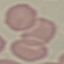
Malaria status: uninfected. Giemsa stain. Cell patch, automatically extracted from a larger field of view and resized to 64 × 64 pixels. Acquired by smartphone through the microscope eyepiece. Thin smear of blood.